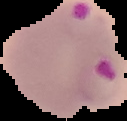
Summary:
  - Preparation: thin blood film
  - Image size: 127×121 pixels
  - Malaria status: parasitized
  - Image type: segmented cell region with the area outside set to black